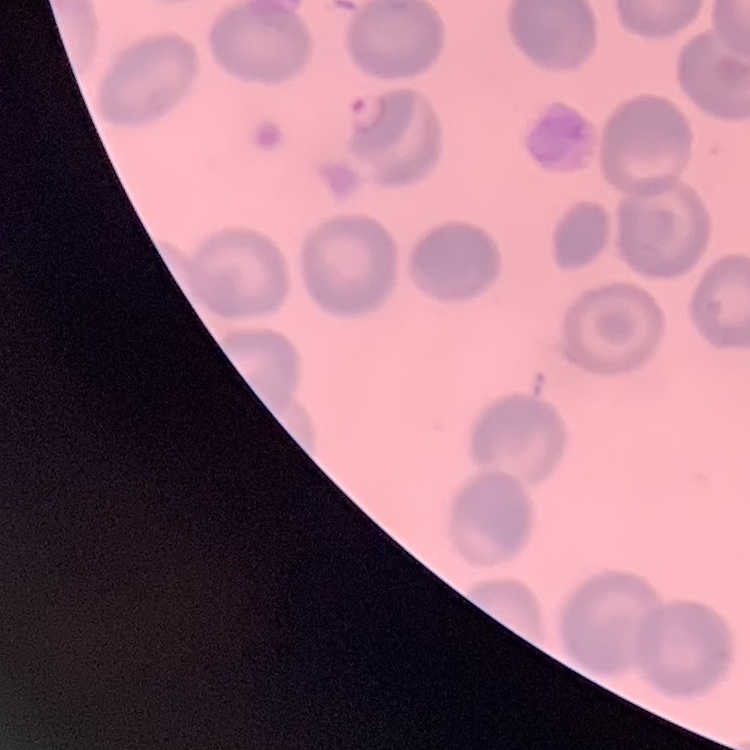 The red blood cells exhibit no rouleaux formation. Thin blood smear. Field's or Giemsa stain. One tile cut from a larger photomicrograph.